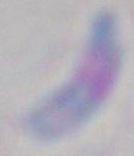 Captured at 1000x magnification. Photomicrograph. Toxoplasma gondii is seen.